Identify the blood parasite species.
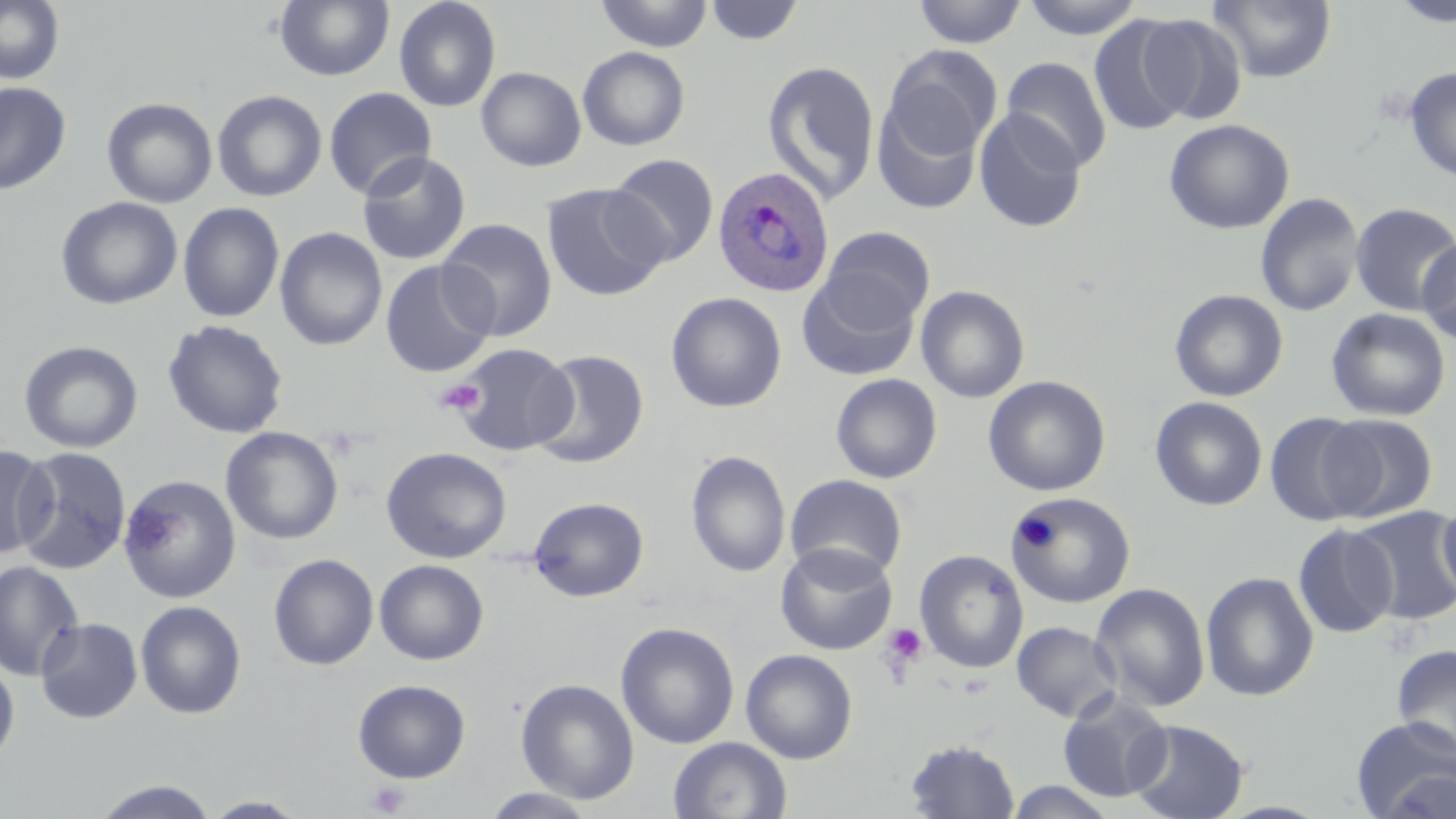
Plasmodium ovale.

Approximate bounding boxes as named x1/y1/x2/y2 corners in pixels. Platelet locations: (x1=434, y1=377, x2=486, y2=417), (x1=1013, y1=515, x2=1060, y2=552), (x1=880, y1=622, x2=929, y2=671), (x1=364, y1=781, x2=411, y2=817). Plasmodium ovale-infected red blood cell locations: (x1=711, y1=166, x2=834, y2=297). Uninfected red blood cell locations: (x1=0, y1=0, x2=65, y2=85), (x1=274, y1=0, x2=394, y2=82), (x1=393, y1=0, x2=501, y2=112), (x1=594, y1=0, x2=714, y2=52), (x1=911, y1=0, x2=1028, y2=48), (x1=1020, y1=0, x2=1145, y2=40), (x1=1208, y1=0, x2=1337, y2=83), (x1=1388, y1=0, x2=1456, y2=27), (x1=704, y1=1, x2=804, y2=46), (x1=1135, y1=13, x2=1247, y2=125), (x1=1088, y1=15, x2=1196, y2=136), (x1=882, y1=45, x2=1001, y2=160), (x1=577, y1=46, x2=690, y2=150), (x1=1001, y1=57, x2=1112, y2=172), (x1=762, y1=59, x2=881, y2=205), (x1=476, y1=66, x2=586, y2=172), (x1=1404, y1=66, x2=1456, y2=182), (x1=0, y1=82, x2=71, y2=195), (x1=323, y1=87, x2=437, y2=199), (x1=212, y1=89, x2=327, y2=201), (x1=101, y1=97, x2=218, y2=208), (x1=872, y1=100, x2=983, y2=215), (x1=973, y1=107, x2=1087, y2=233), (x1=1164, y1=118, x2=1295, y2=234), (x1=356, y1=151, x2=471, y2=266), (x1=606, y1=154, x2=719, y2=267), (x1=541, y1=182, x2=669, y2=302), (x1=1255, y1=193, x2=1364, y2=317), (x1=55, y1=196, x2=183, y2=310), (x1=178, y1=202, x2=285, y2=323), (x1=1350, y1=202, x2=1456, y2=316), (x1=437, y1=218, x2=557, y2=341), (x1=275, y1=226, x2=388, y2=351), (x1=819, y1=226, x2=935, y2=328), (x1=1416, y1=237, x2=1456, y2=345), (x1=380, y1=259, x2=496, y2=378), (x1=797, y1=271, x2=921, y2=382), (x1=915, y1=284, x2=1030, y2=403), (x1=1169, y1=288, x2=1289, y2=402), (x1=665, y1=292, x2=787, y2=413), (x1=1325, y1=307, x2=1451, y2=421), (x1=162, y1=319, x2=289, y2=439), (x1=18, y1=340, x2=144, y2=454), (x1=449, y1=342, x2=578, y2=456), (x1=531, y1=349, x2=649, y2=469), (x1=830, y1=373, x2=943, y2=484), (x1=983, y1=375, x2=1110, y2=496), (x1=1150, y1=396, x2=1268, y2=511), (x1=1264, y1=410, x2=1375, y2=526), (x1=1318, y1=414, x2=1439, y2=523), (x1=220, y1=427, x2=343, y2=545), (x1=0, y1=444, x2=55, y2=559), (x1=12, y1=446, x2=132, y2=575), (x1=381, y1=446, x2=512, y2=563), (x1=685, y1=450, x2=791, y2=577), (x1=784, y1=474, x2=908, y2=580), (x1=118, y1=475, x2=241, y2=603), (x1=1007, y1=492, x2=1137, y2=609), (x1=528, y1=497, x2=649, y2=601), (x1=1437, y1=497, x2=1456, y2=606), (x1=1350, y1=507, x2=1455, y2=626), (x1=1292, y1=524, x2=1398, y2=638), (x1=775, y1=542, x2=898, y2=655), (x1=914, y1=549, x2=1029, y2=674), (x1=268, y1=553, x2=379, y2=670), (x1=374, y1=559, x2=489, y2=665), (x1=0, y1=561, x2=84, y2=681), (x1=1200, y1=571, x2=1319, y2=702), (x1=1090, y1=582, x2=1211, y2=712), (x1=135, y1=600, x2=247, y2=719), (x1=35, y1=617, x2=143, y2=723), (x1=1011, y1=621, x2=1122, y2=723), (x1=615, y1=622, x2=740, y2=749), (x1=1392, y1=644, x2=1456, y2=757), (x1=740, y1=648, x2=858, y2=763), (x1=0, y1=656, x2=19, y2=765), (x1=352, y1=678, x2=471, y2=783), (x1=516, y1=678, x2=639, y2=804), (x1=1057, y1=690, x2=1172, y2=803), (x1=1351, y1=717, x2=1456, y2=819), (x1=1125, y1=718, x2=1249, y2=819), (x1=668, y1=736, x2=793, y2=819), (x1=903, y1=738, x2=1021, y2=819), (x1=90, y1=779, x2=221, y2=818), (x1=1002, y1=779, x2=1120, y2=818), (x1=480, y1=788, x2=601, y2=818), (x1=201, y1=796, x2=311, y2=818). Thin blood film. Optical microscopy. May-Grünwald-Giemsa-stained preparation. One field of a larger specimen. Image is 1456×819 pixels. Captured at 1000x magnification.